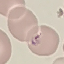

Malaria status: parasitized. Cell patch, automatically extracted from a larger field of view and resized to 64 × 64 pixels. Acquired by smartphone through the microscope eyepiece. Giemsa stain. Thin smear of blood.